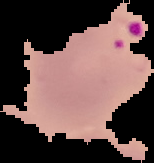
Summary:
  - Result: Plasmodium parasites identified
  - Image size: 154×163 pixels
  - Image type: cell region segmented out of the field of view; surrounding area masked to black
  - Preparation: thin blood film